State which cell type is depicted.
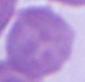

This is an erythrocyte.

magnification = 1000x
modality = micrograph